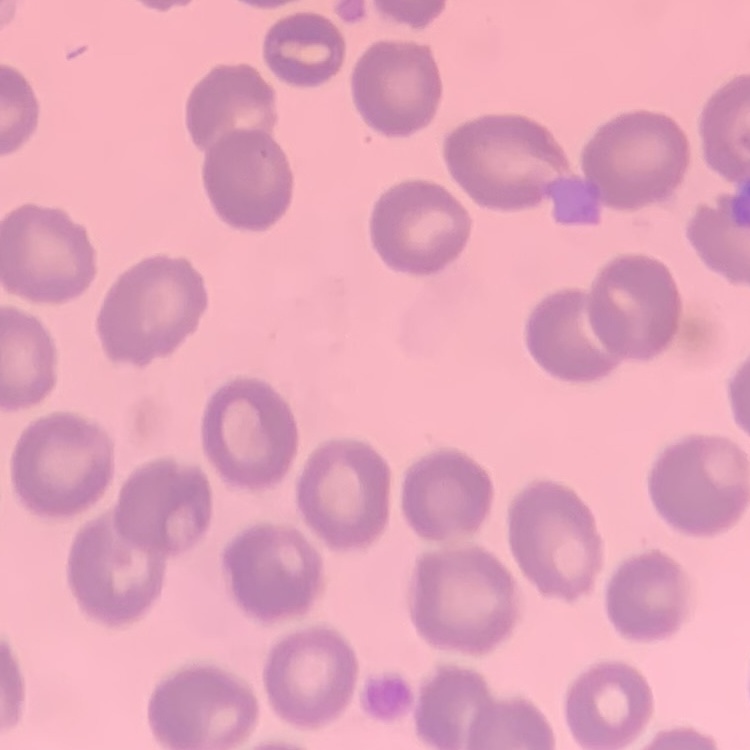
The erythrocytes show no rouleaux formation. Thin blood smear. Field's or Giemsa stain. One tile cut from a larger photomicrograph.